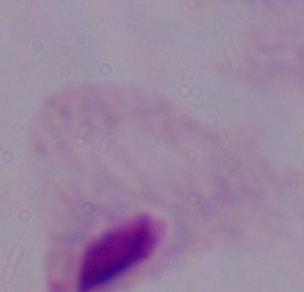
Photomicrograph. A trichomonad is shown. Captured at 1000x magnification.